Locate and identify every blood parasite.
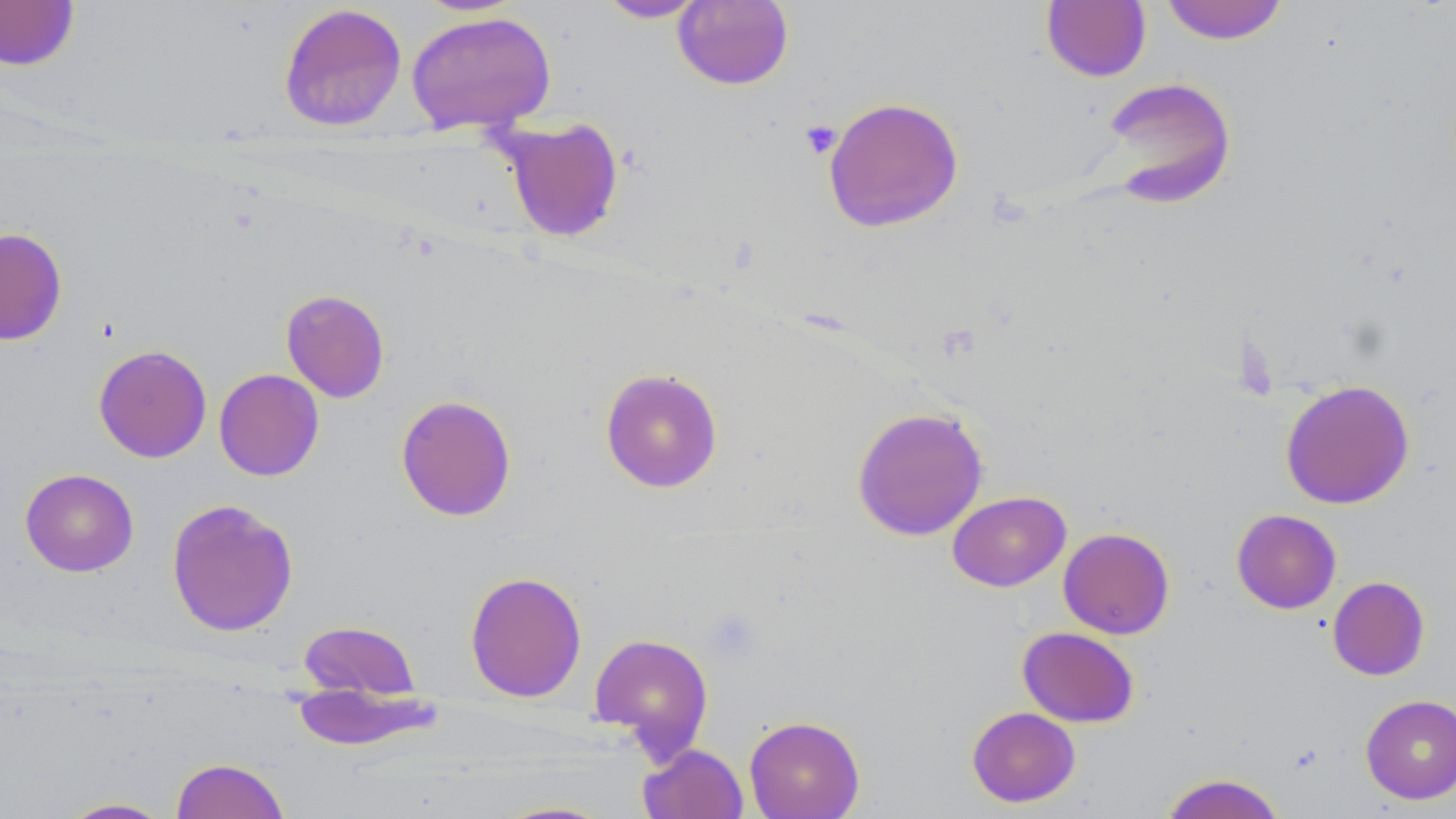

No blood parasites seen.

slide-level diagnosis = no evidence of blood parasites
preparation = thin blood smear
field of view = one of a larger specimen
magnification = 1000x
modality = optical microscopy
platelet locations = approximate bounding boxes as named x1/y1/x2/y2 corners in pixels: (x1=800, y1=119, x2=842, y2=159), (x1=703, y1=608, x2=761, y2=664)
image size = 1456×819 pixels
uninfected red blood cell locations = approximate bounding boxes as named x1/y1/x2/y2 corners in pixels: (x1=596, y1=0, x2=710, y2=23), (x1=1160, y1=0, x2=1289, y2=44), (x1=0, y1=1, x2=80, y2=71), (x1=672, y1=1, x2=794, y2=90), (x1=1041, y1=1, x2=1151, y2=82), (x1=278, y1=3, x2=407, y2=132), (x1=405, y1=11, x2=556, y2=134), (x1=1101, y1=76, x2=1237, y2=206), (x1=823, y1=96, x2=964, y2=233), (x1=497, y1=116, x2=625, y2=242), (x1=0, y1=227, x2=67, y2=346), (x1=280, y1=289, x2=390, y2=403), (x1=93, y1=344, x2=212, y2=463), (x1=600, y1=367, x2=723, y2=492), (x1=214, y1=368, x2=324, y2=481), (x1=1280, y1=379, x2=1415, y2=510), (x1=395, y1=394, x2=517, y2=521), (x1=851, y1=406, x2=989, y2=541), (x1=20, y1=468, x2=139, y2=577), (x1=947, y1=490, x2=1071, y2=592), (x1=166, y1=498, x2=299, y2=637), (x1=1231, y1=509, x2=1341, y2=614), (x1=1058, y1=527, x2=1175, y2=639), (x1=464, y1=570, x2=587, y2=702), (x1=1327, y1=576, x2=1430, y2=680), (x1=298, y1=620, x2=420, y2=699), (x1=1017, y1=626, x2=1140, y2=727), (x1=588, y1=632, x2=714, y2=759), (x1=291, y1=683, x2=444, y2=752), (x1=1361, y1=694, x2=1456, y2=804), (x1=966, y1=706, x2=1081, y2=808), (x1=744, y1=715, x2=866, y2=819), (x1=637, y1=743, x2=749, y2=819), (x1=170, y1=757, x2=289, y2=819), (x1=1160, y1=773, x2=1287, y2=819), (x1=57, y1=797, x2=175, y2=818), (x1=490, y1=800, x2=619, y2=819)
stain = May-Grünwald-Giemsa